State which parasite is depicted.
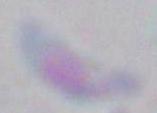

Toxoplasma gondii.

Photomicrograph. Captured at 1000x magnification.